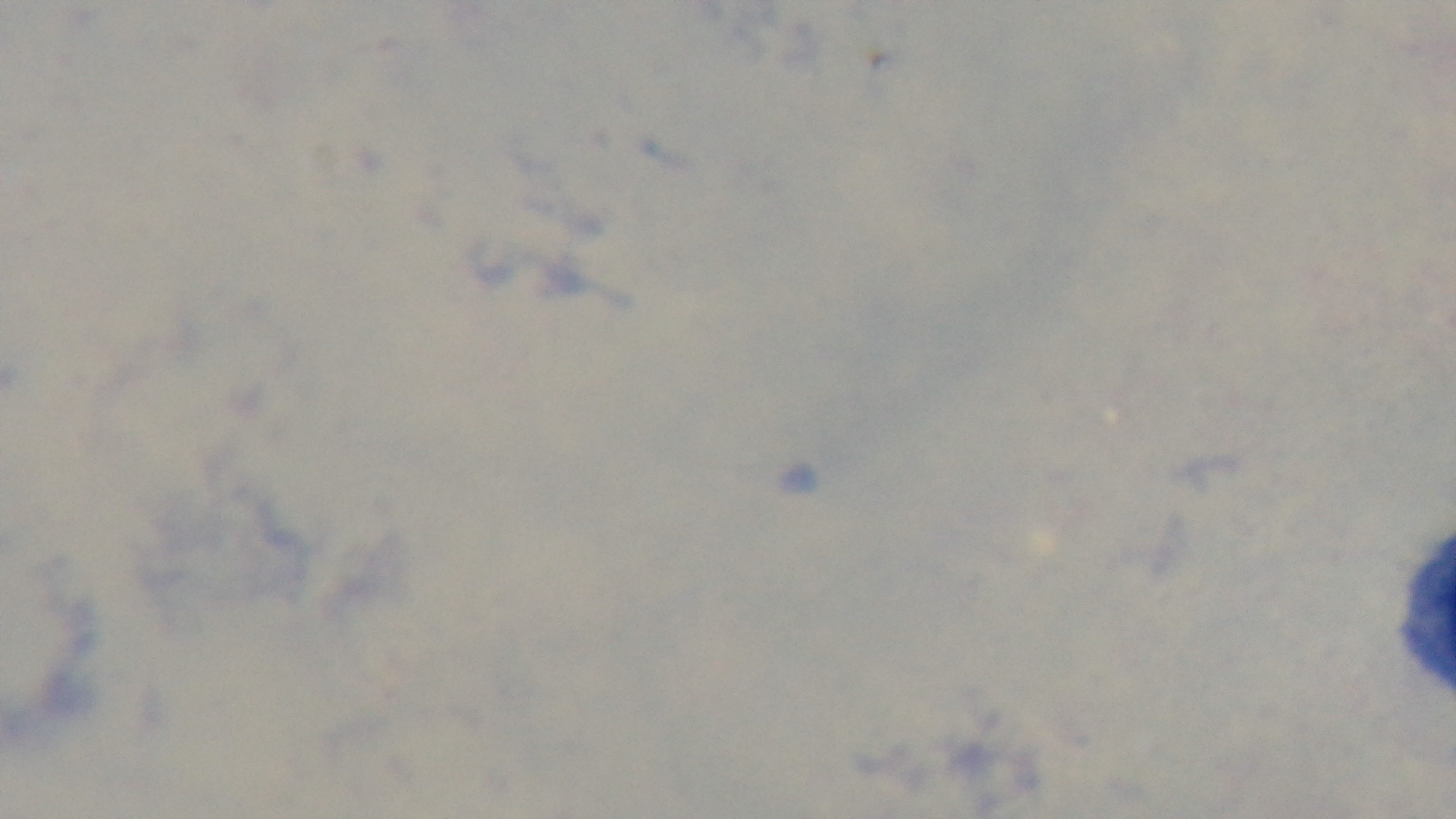
preparation = thick
field of view = single
modality = light microscopy
malaria status = negative
objective = 100x oil immersion
capture = mounted 4K digital camera
stain = Giemsa